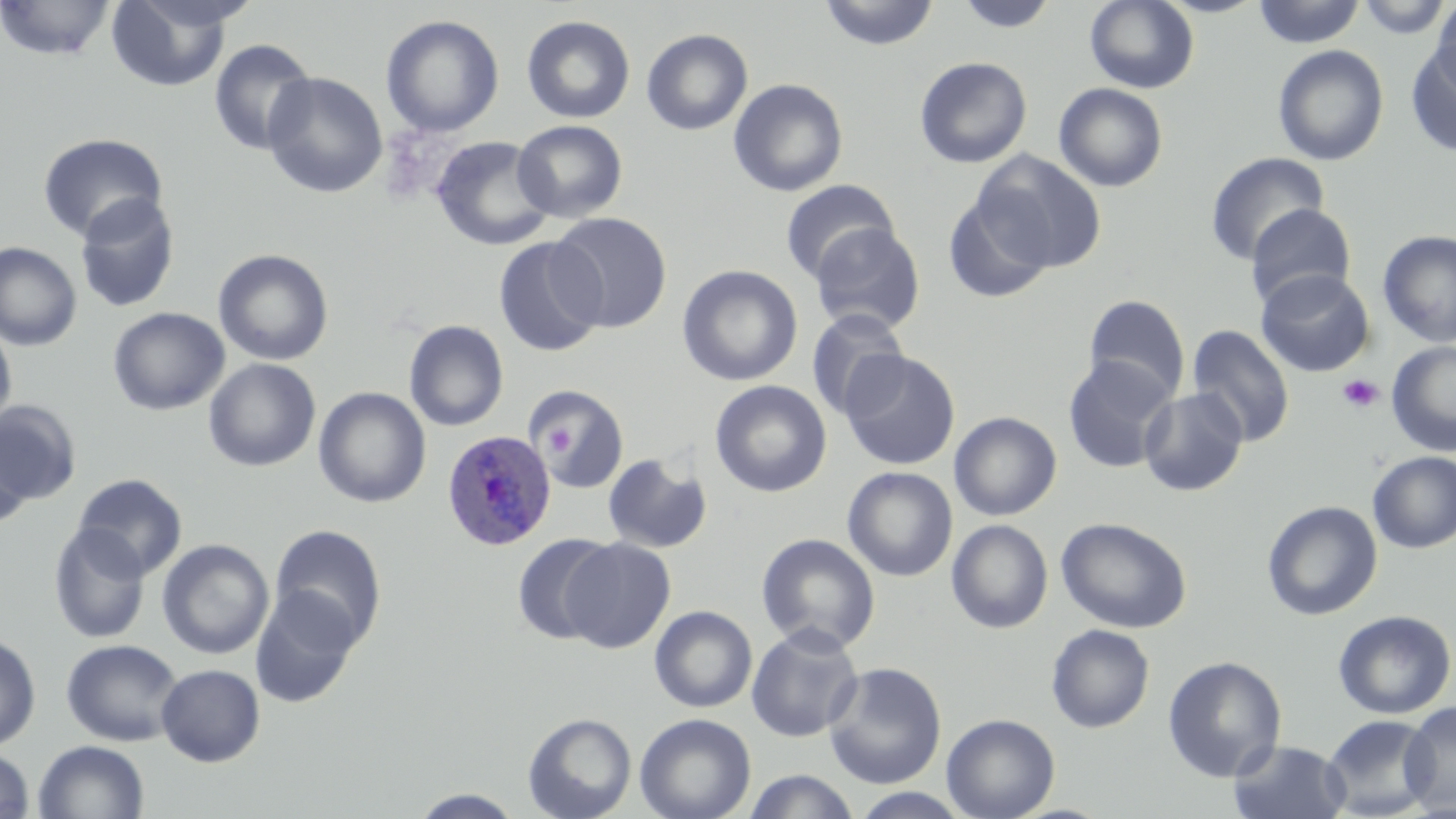
{
  "slide_level_diagnosis": "Plasmodium ovale",
  "image_size": "1456×819 pixels",
  "magnification": "1000x",
  "stain": "May-Grünwald-Giemsa",
  "preparation": "thin blood film",
  "uninfected_red_blood_cell_locations": "approximate bounding boxes as (x1,y1)-(x2,y2) corner pairs in pixels: (0,0)-(116,61), (106,0)-(236,92), (818,0)-(940,50), (1084,0)-(1200,93), (1251,0)-(1365,48), (1355,0)-(1452,39), (1431,0)-(1456,93), (956,1)-(1059,34), (380,14)-(505,138), (521,14)-(636,124), (641,28)-(753,135), (208,38)-(317,155), (1405,43)-(1456,158), (1272,44)-(1389,166), (914,56)-(1032,169), (262,71)-(388,198), (728,78)-(848,197), (1053,82)-(1169,192), (512,120)-(628,223), (38,132)-(168,243), (430,135)-(556,251), (972,150)-(1107,273), (1204,152)-(1329,266), (780,178)-(900,284), (941,191)-(1055,304), (74,194)-(180,314), (1244,202)-(1357,308), (549,211)-(673,333), (809,222)-(926,335), (1377,230)-(1456,348), (493,237)-(607,357), (0,242)-(82,352), (213,249)-(333,366), (678,264)-(803,386), (1255,269)-(1375,377), (1083,294)-(1191,402), (108,307)-(230,416), (805,309)-(910,420), (0,318)-(17,434), (404,320)-(509,432), (1186,324)-(1295,447), (1386,341)-(1456,456), (839,350)-(960,470), (1062,355)-(1177,473), (204,358)-(321,472), (709,380)-(832,498), (531,384)-(629,492), (313,387)-(431,508), (1139,388)-(1248,496), (1,400)-(81,508), (949,411)-(1062,521), (0,424)-(33,531), (1367,451)-(1456,553), (603,452)-(712,554), (842,466)-(958,581), (73,474)-(187,579), (1262,500)-(1383,621), (1056,516)-(1192,633), (947,520)-(1052,633), (48,523)-(151,644), (269,524)-(387,648), (756,532)-(881,654), (511,533)-(616,644), (561,537)-(676,654), (157,539)-(274,659), (251,587)-(362,708), (650,605)-(758,713), (1333,609)-(1456,719), (746,624)-(864,742), (1046,624)-(1155,733), (0,632)-(41,750), (61,639)-(183,746), (1162,655)-(1287,782), (823,661)-(947,789), (156,664)-(265,766), (1400,700)-(1456,815), (523,712)-(637,819), (634,713)-(756,819), (941,713)-(1060,819), (1321,715)-(1438,819), (1229,739)-(1351,819), (33,740)-(150,819), (0,748)-(35,819), (742,769)-(861,818), (410,788)-(525,818), (850,788)-(972,818)",
  "platelet_locations": "approximate bounding boxes as (x1,y1)-(x2,y2) corner pairs in pixels: (1337,373)-(1384,414), (541,424)-(575,459)",
  "plasmodium_ovale_infected_red_blood_cell_locations": "approximate bounding boxes as (x1,y1)-(x2,y2) corner pairs in pixels: (442,430)-(556,551)",
  "field_of_view": "single",
  "modality": "optical microscopy"
}